Name the parasite shown.
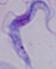
A trypanosome.

Summary:
  - Magnification: 1000x
  - Modality: micrograph